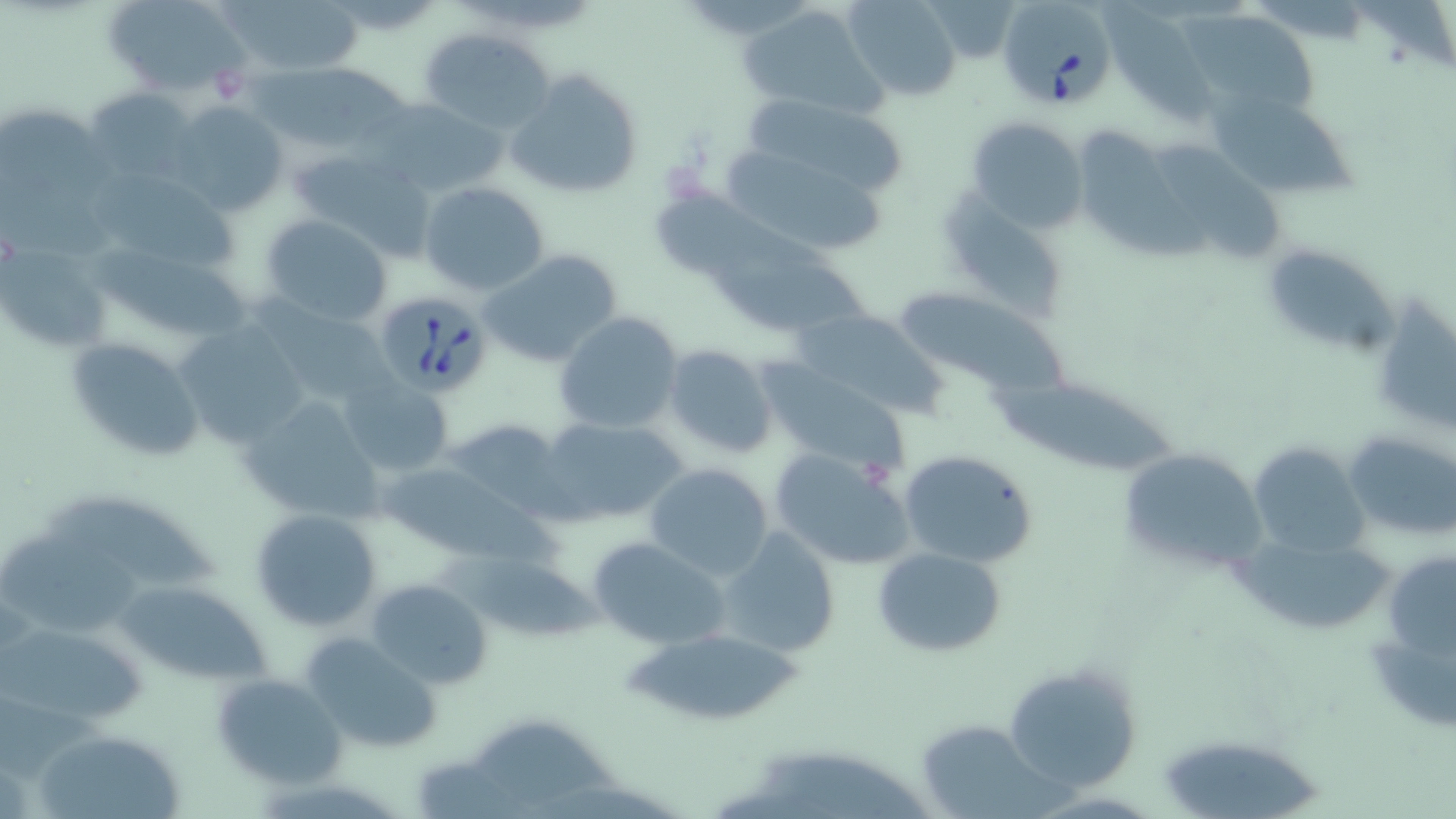
{
  "slide_level_diagnosis": "Babesia divergens",
  "uninfected_red_blood_cell_locations": "approximate bounding boxes as (x1,y1)-(x2,y2) corner pairs in pixels: (100,0)-(252,98), (218,0)-(366,79), (842,0)-(961,100), (931,0)-(1020,55), (1103,2)-(1223,127), (739,4)-(886,116), (1177,7)-(1322,119), (420,29)-(555,132), (237,54)-(424,147), (505,69)-(642,201), (83,87)-(199,187), (739,91)-(916,206), (373,98)-(511,200), (167,101)-(287,218), (1212,103)-(1360,197), (966,115)-(1089,231), (1082,133)-(1218,263), (285,146)-(428,249), (1160,147)-(1283,268), (722,153)-(888,257), (95,169)-(243,276), (418,180)-(551,296), (654,189)-(828,278), (942,190)-(1066,317), (257,214)-(394,328), (95,242)-(251,347), (1263,245)-(1397,352), (2,246)-(110,352), (479,249)-(621,366), (707,253)-(871,334), (900,287)-(1074,403), (248,292)-(401,404), (1373,304)-(1456,436), (791,308)-(947,419), (552,311)-(685,435), (175,319)-(311,449), (64,336)-(206,465), (662,344)-(776,460), (757,364)-(905,470), (338,377)-(453,477), (994,384)-(1186,478), (238,392)-(388,527), (538,416)-(685,524), (442,417)-(568,517), (1344,430)-(1456,542), (1246,440)-(1368,557), (1117,446)-(1266,577), (770,448)-(915,571), (898,449)-(1038,567), (377,461)-(532,558), (644,462)-(774,579), (41,499)-(223,592), (249,508)-(381,630), (717,527)-(841,657), (0,534)-(152,633), (587,534)-(733,650), (1244,535)-(1393,634), (871,546)-(1006,657), (467,551)-(599,645), (1392,558)-(1456,666), (365,577)-(492,692), (120,581)-(271,683), (1,617)-(151,729), (623,626)-(809,727), (300,633)-(444,752), (1002,659)-(1142,792), (210,673)-(344,787), (915,720)-(1056,819), (472,721)-(621,810), (33,734)-(185,819), (1159,743)-(1316,819)",
  "image_size": "1456×819 pixels",
  "babesia_divergens_infected_red_blood_cell_locations": "approximate bounding boxes as (x1,y1)-(x2,y2) corner pairs in pixels: (996,0)-(1119,113), (377,291)-(496,398)",
  "magnification": "1000x",
  "modality": "optical microscopy",
  "stain": "May-Grünwald-Giemsa",
  "preparation": "thin blood smear",
  "field_of_view": "one of a larger specimen"
}